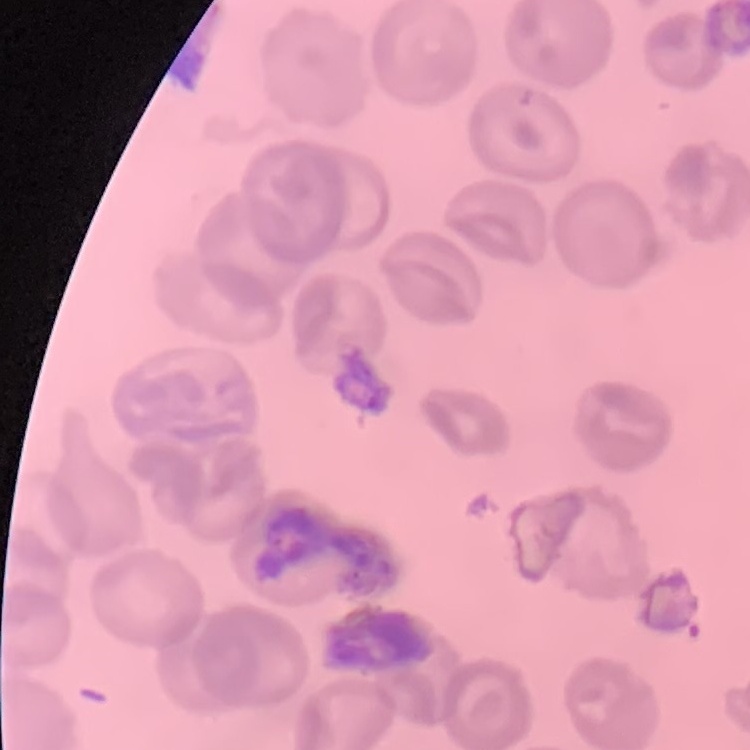

erythrocyte morphology = no rouleaux formation
preparation = thin blood smear
stain = Field's or Giemsa
image type = square crop of a larger photomicrograph